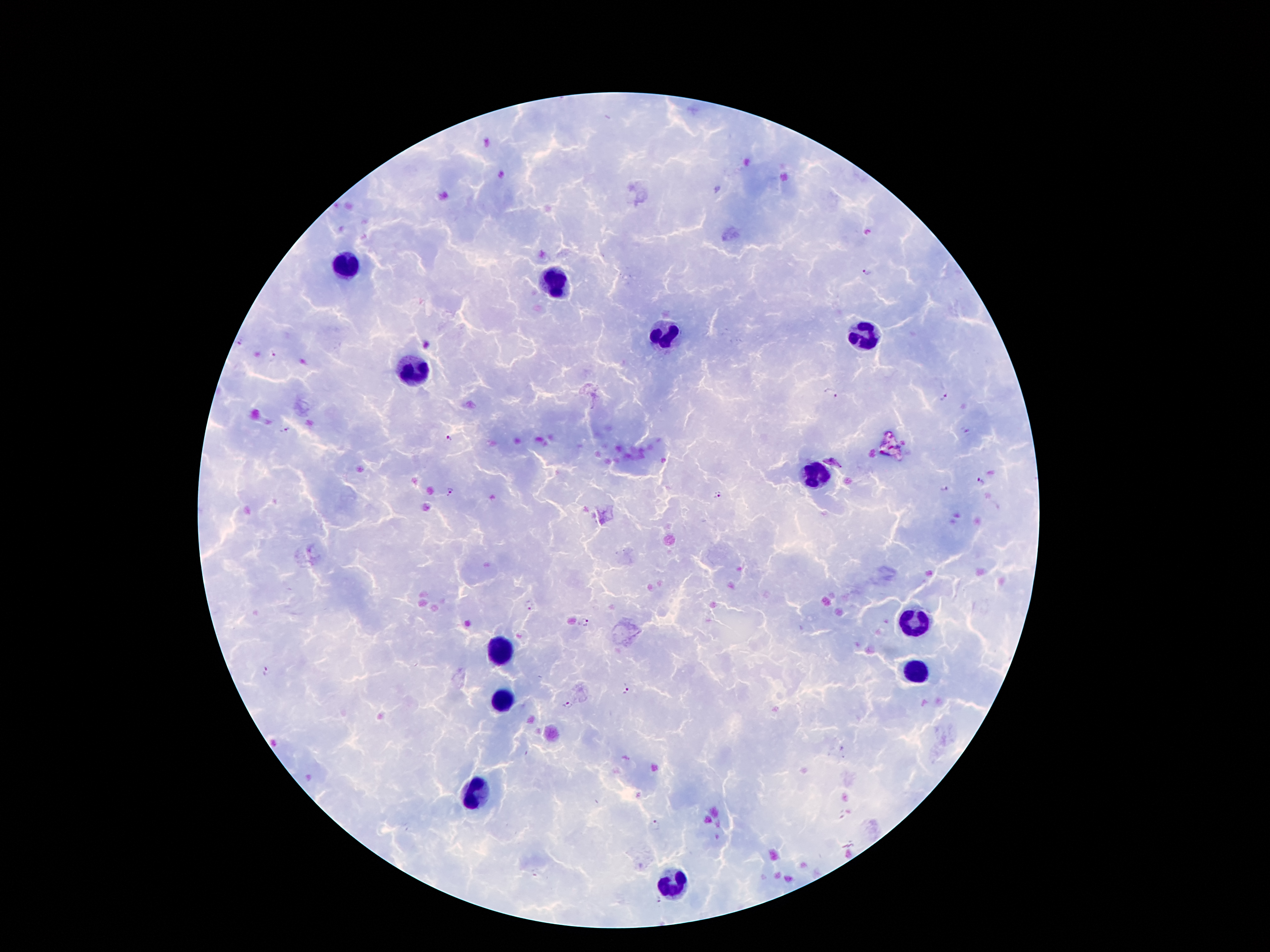 Approximate centers as (x, y) in pixels. Leukocyte locations: (350, 266), (561, 284), (668, 337), (864, 337), (412, 368), (816, 477), (916, 625), (501, 650), (915, 673), (503, 697), (477, 793), (673, 885). Plasmodium parasite locations: (866, 271), (237, 343), (274, 357), (832, 394), (944, 397), (284, 428), (965, 433), (448, 439), (833, 461), (982, 480), (945, 490), (450, 491), (717, 495), (528, 606), (583, 621), (267, 671), (627, 690), (568, 706), (656, 824), (659, 900). Thick blood smear. 100x magnification. Photographed through the microscope eyepiece with a smartphone camera. One field from this slide. Image is 1270×952 pixels. Giemsa-stained preparation. Patient malaria status: infected with Plasmodium falciparum.